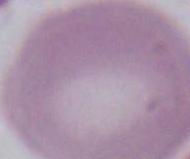 A red blood cell is shown. Photomicrograph. 1000x magnification.